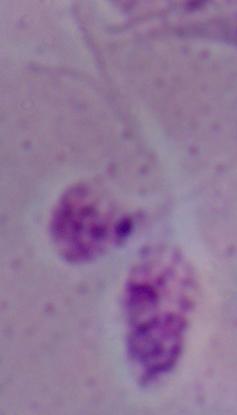

Photomicrograph. A Leishmania parasite is shown. Captured at 1000x magnification.